State which cell type is depicted.
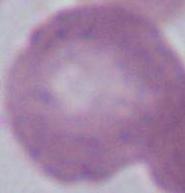
An erythrocyte.

1000x magnification. Photomicrograph.